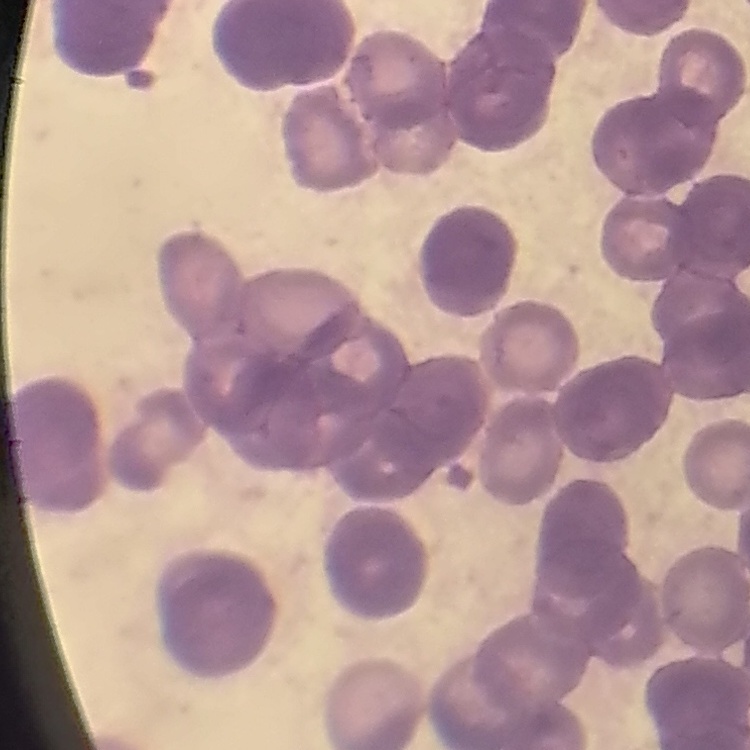
{
  "erythrocyte_morphology": "rouleaux formation",
  "image_type": "one tile cut from a larger photomicrograph",
  "stain": "Field's or Giemsa",
  "preparation": "thin blood film"
}